Evaluate for Plasmodium parasites.
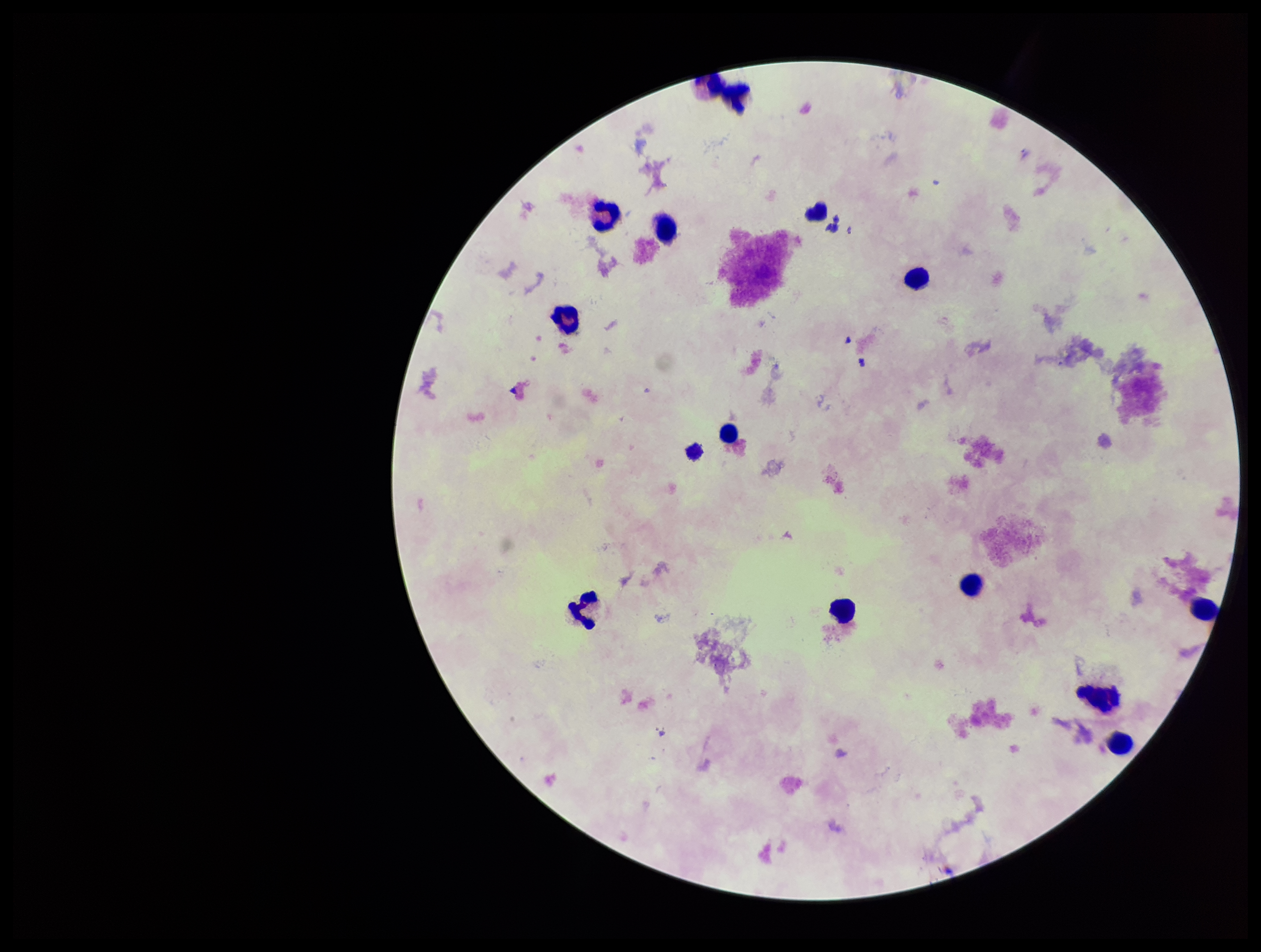

None identified.

leukocyte count = 14
patient malaria status = negative
field of view = single
preparation = thick
image size = 1261×952 pixels
parasite count = 0
stain = Giemsa
capture = smartphone photograph through the microscope eyepiece